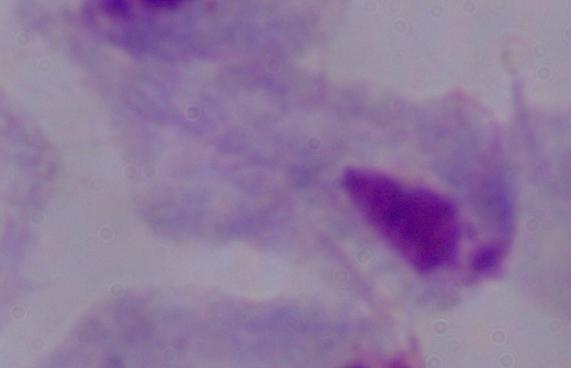

Summary:
  - Identification: trichomonad
  - Modality: photomicrograph
  - Magnification: 1000x